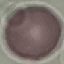
Malaria status: uninfected. Photographed with a smartphone camera at the microscope eyepiece. Giemsa stain. Cell patch, automatically extracted from a larger field of view and resized to 64 × 64 pixels. Thin smear of blood.